Classify this cell by malaria status.
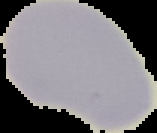
It is uninfected.

Image is 157×133 pixels. From a thin blood smear. The area outside the segmented cell region is set to black.